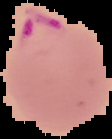

Summary:
  - Image size: 112×139 pixels
  - Malaria status: parasitized
  - Preparation: thin blood film
  - Image type: segmented cell region with the area outside set to black